Report the malaria status.
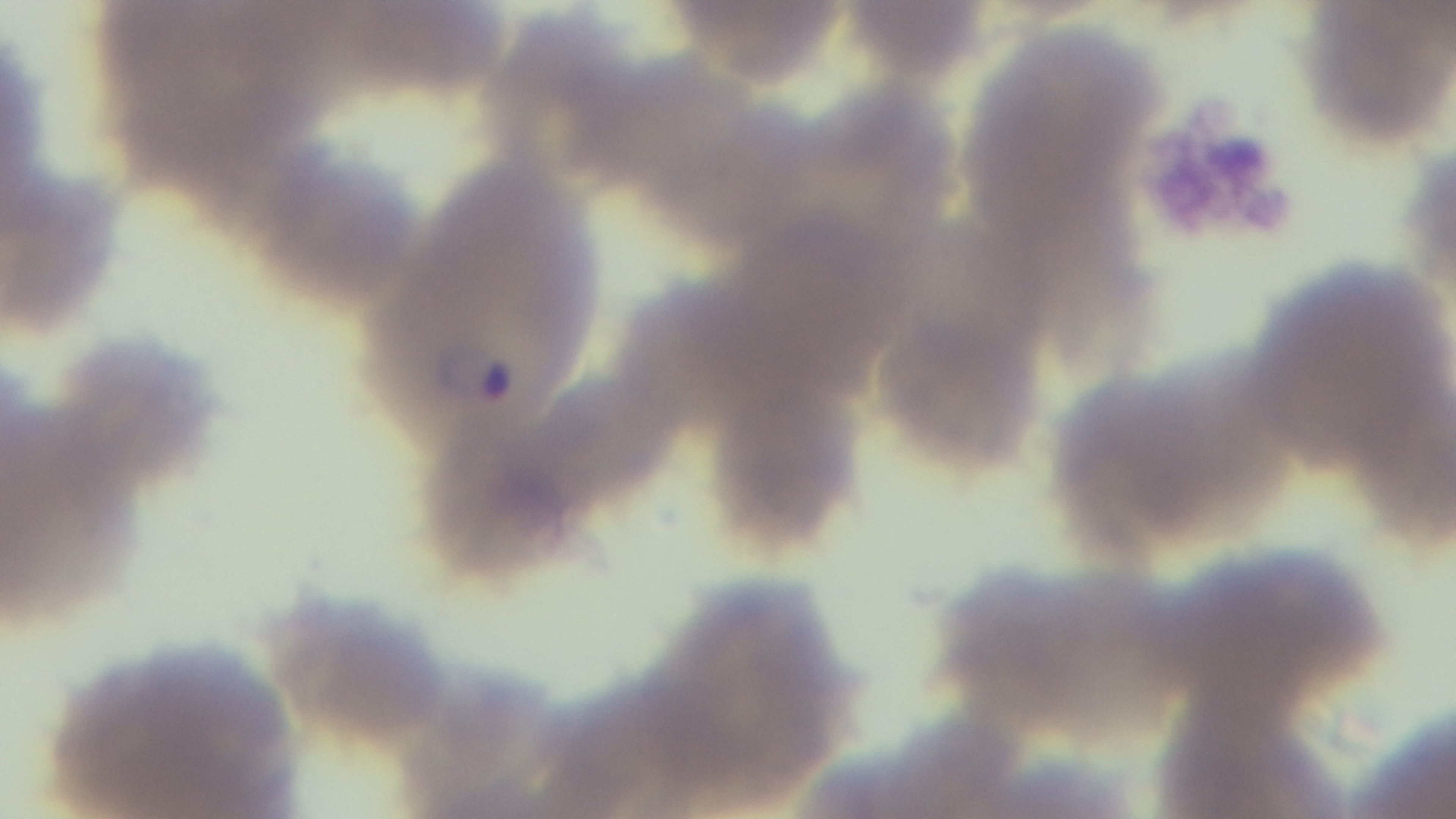

Infected.

Summary:
  - Stain: Giemsa
  - Preparation: thin
  - Modality: light microscopy
  - Field of view: one from the slide
  - Capture: mounted 4K digital camera
  - Objective: 100x oil immersion